Assess the morphology of the red blood cells.
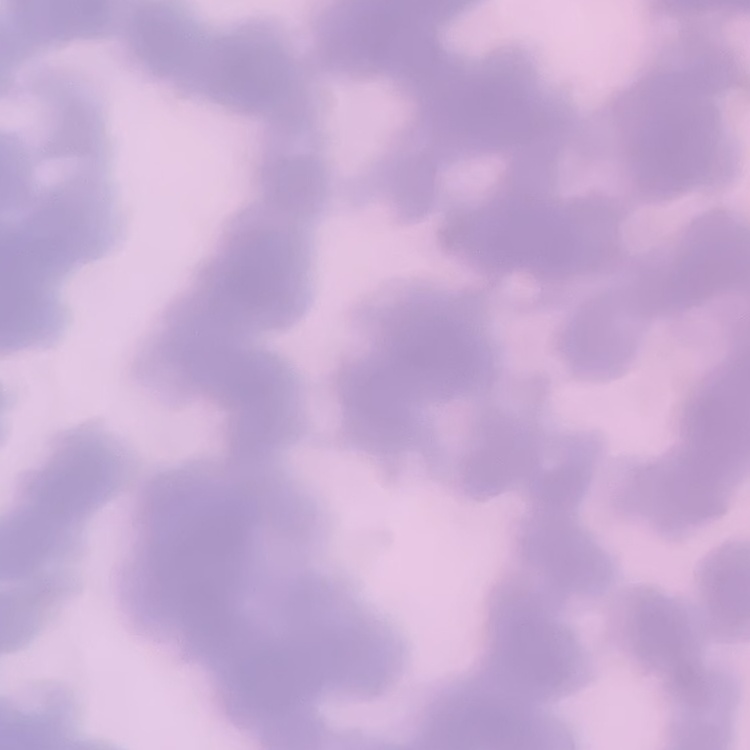
Rouleaux formation.

One tile cut from a larger photomicrograph. Stained with either Field's or Giemsa. Thin blood film.